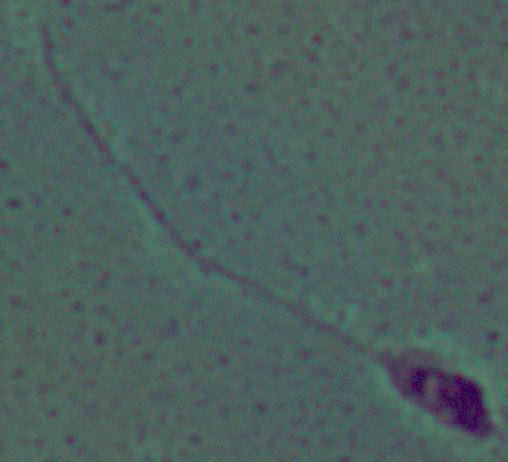

A Leishmania parasite is shown. Captured at 1000x magnification. Micrograph.